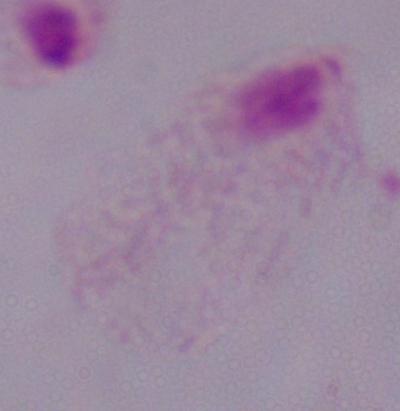

Summary:
  - Magnification: 1000x
  - Modality: photomicrograph
  - Identification: trichomonad